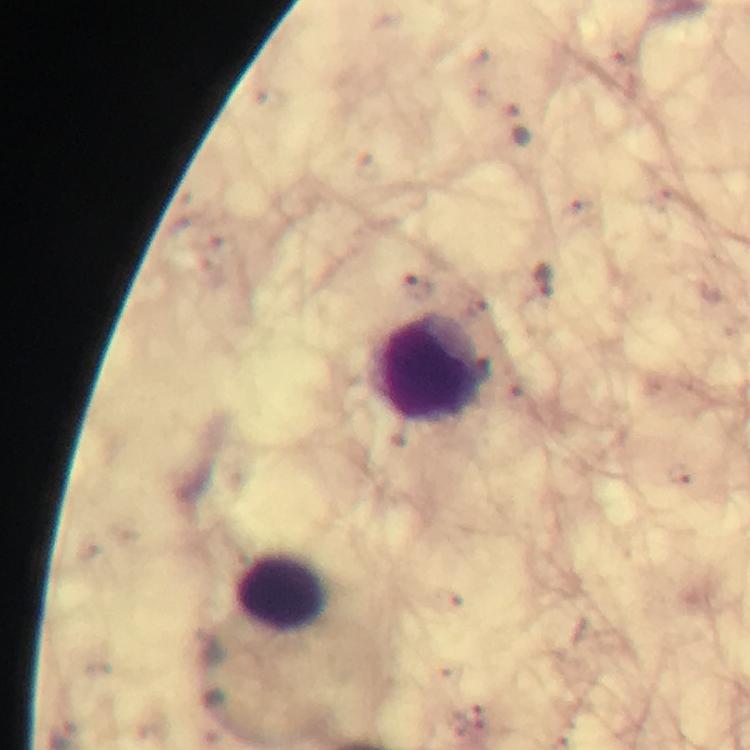
Approximate centers as [x, y] in pixels.
Summary:
  - Leukocyte locations: [432, 372], [285, 592]
  - Image size: 750×750 pixels
  - Cropped from: a single field of view
  - Magnification: 100x
  - Capture: smartphone photograph through a microscope
  - Stain: Giemsa
  - Preparation: thick blood film
  - Plasmodium parasites: none seen
  - Context: from a malaria diagnostic workup
  - Immersion oil: used